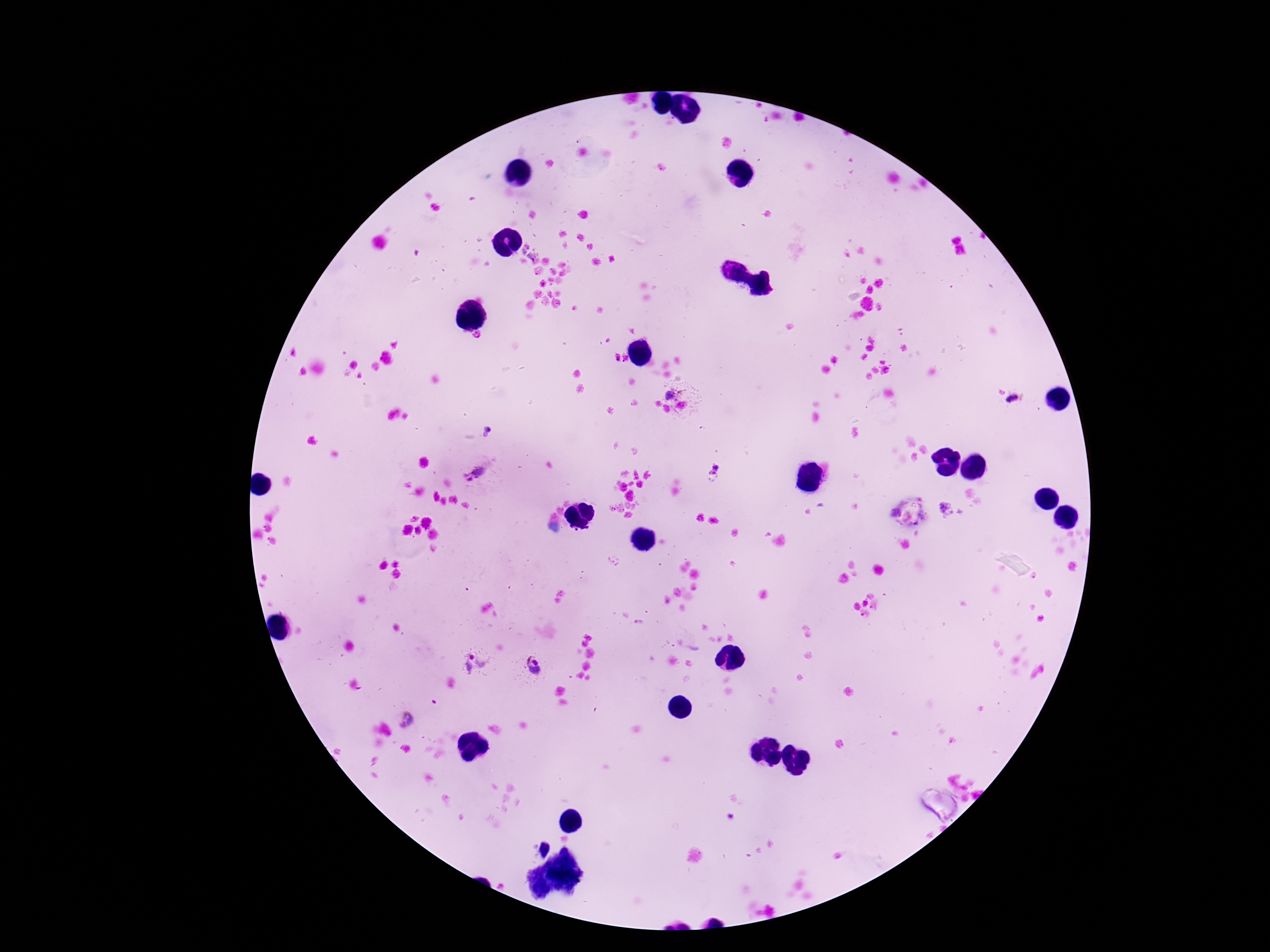

Approximate object centers, in pixels from the top-left corner.
Summary:
  - Plasmodium parasite locations: (x=616, y=356), (x=625, y=358), (x=672, y=394), (x=1013, y=400), (x=487, y=428), (x=485, y=435), (x=479, y=471), (x=714, y=472), (x=945, y=509), (x=474, y=662), (x=535, y=667), (x=409, y=717)
  - Capture: smartphone camera through the microscope eyepiece
  - Patient malaria status: positive
  - Magnification: 100x
  - Preparation: thick blood film
  - Field of view: one from this slide
  - Stain: Giemsa
  - Image size: 1270×952 pixels